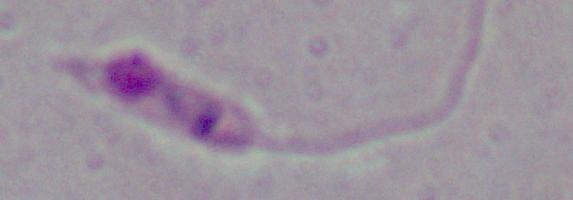
A Leishmania parasite is seen. Captured at 1000x magnification. Photomicrograph.